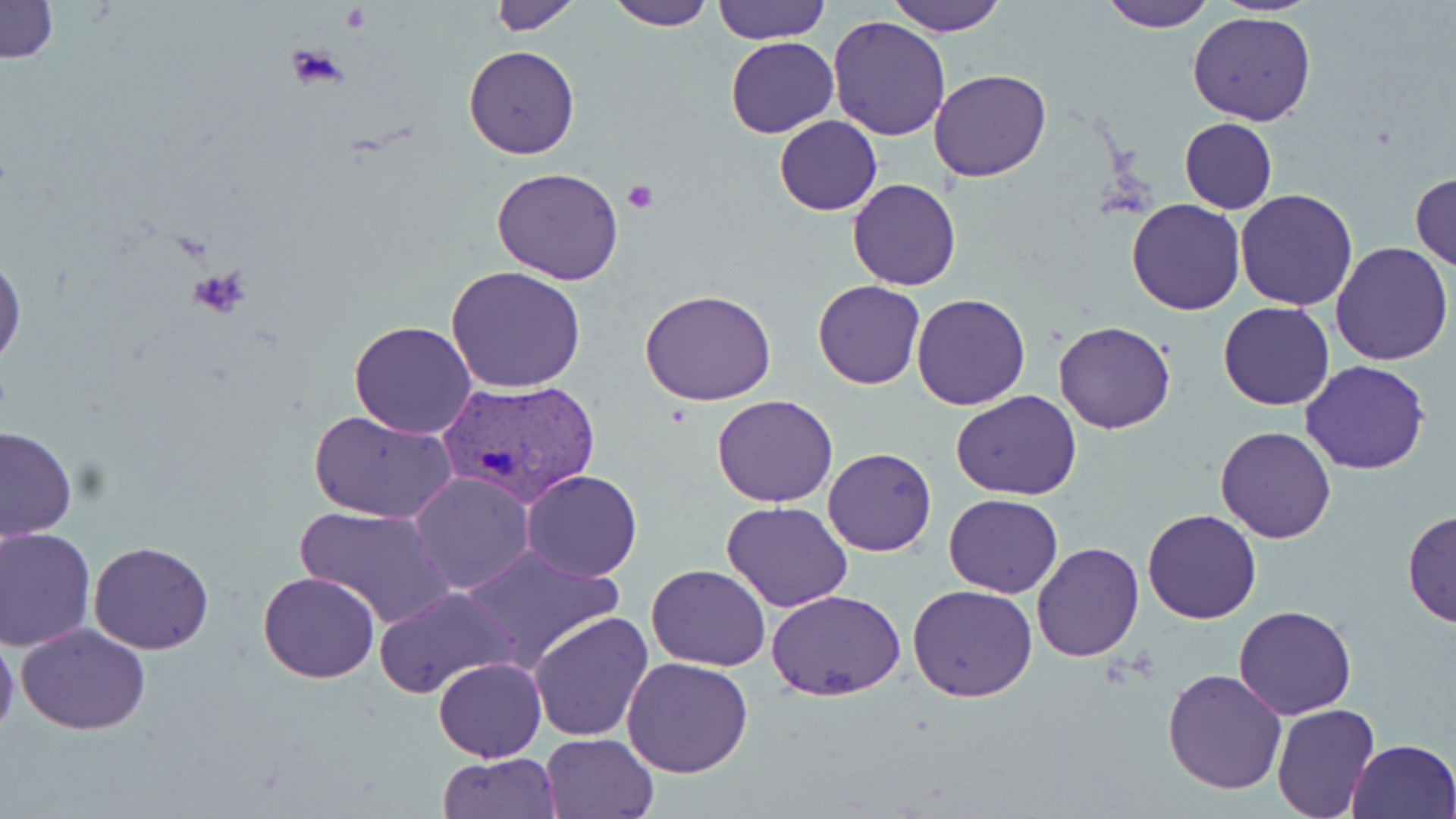 Approximate bounding boxes as (x1,y1)-(x2,y2) corner pairs in pixels. Plasmodium vivax-infected red blood cell locations: (439,376)-(600,504). Uninfected red blood cell locations: (606,0)-(713,30), (713,0)-(830,45), (888,0)-(1007,36), (1101,0)-(1217,29), (1207,0)-(1324,14), (0,1)-(59,65), (488,1)-(580,34), (1189,12)-(1318,125), (825,15)-(951,139), (726,36)-(838,139), (463,45)-(580,160), (929,68)-(1052,182), (773,116)-(883,216), (1178,118)-(1278,214), (491,167)-(623,283), (1411,172)-(1456,272), (848,178)-(961,290), (1235,189)-(1360,311), (1127,198)-(1248,315), (1331,243)-(1454,367), (0,253)-(25,372), (445,265)-(588,394), (813,279)-(925,389), (639,289)-(776,405), (912,293)-(1030,411), (1218,301)-(1334,412), (348,319)-(478,439), (1054,320)-(1177,434), (1301,360)-(1431,475), (951,390)-(1081,500), (713,395)-(838,508), (309,410)-(458,524), (0,424)-(76,538), (1215,425)-(1336,543), (823,447)-(936,557), (520,469)-(643,582), (407,471)-(534,594), (943,494)-(1064,598), (722,501)-(852,612), (295,504)-(454,629), (1402,508)-(1456,631), (1142,510)-(1262,624), (0,528)-(96,651), (89,541)-(214,655), (1032,541)-(1143,661), (458,546)-(623,671), (648,563)-(769,672), (258,569)-(380,683), (908,584)-(1038,702), (372,586)-(519,699), (765,588)-(906,702), (1234,604)-(1357,719), (528,610)-(654,741), (15,623)-(152,733), (0,627)-(19,741), (621,656)-(753,776), (433,657)-(546,762), (1163,667)-(1288,794), (1270,705)-(1379,817), (541,733)-(657,818), (1345,738)-(1455,819), (439,752)-(562,818). Platelet locations: (284,47)-(348,88), (623,182)-(657,214), (189,268)-(250,321). Slide-level diagnosis: Plasmodium vivax. Light microscopy. Single field of view. Thin blood smear. May-Grünwald-Giemsa stain. Image is 1456×819 pixels. Captured at 1000x magnification.